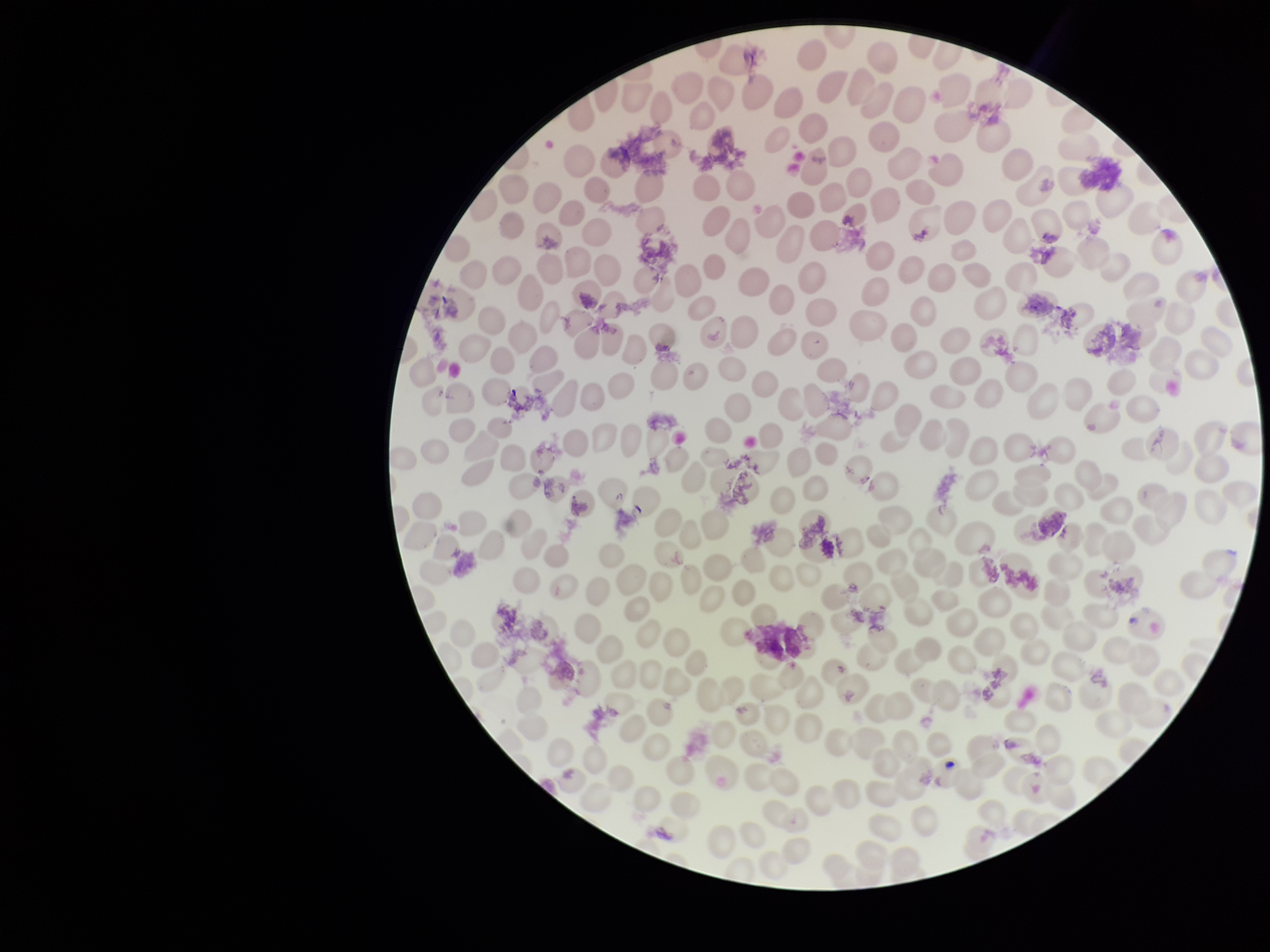

Preparation: thin smear. Parasitized red blood cell count: 0. Image is 1270×952 pixels. Giemsa stain. Parasitized red blood cells: none seen. Single field of view. Patient malaria status: negative. Photographed through the microscope eyepiece with a smartphone camera. Red blood cell count: 174.